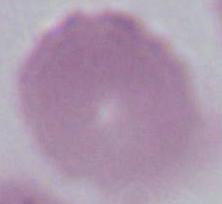

Captured at 1000x magnification. An erythrocyte is shown. Micrograph.